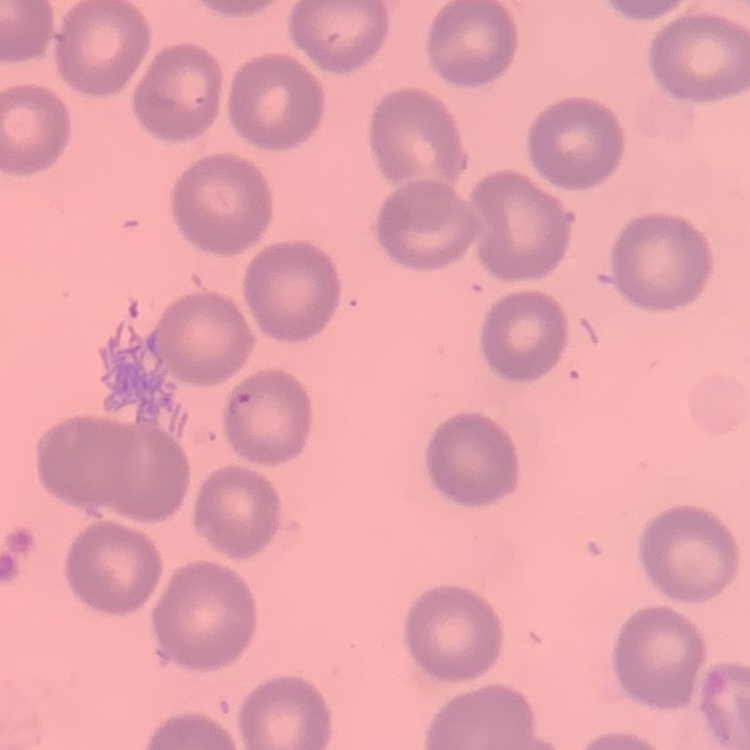

red_blood_cell_morphology: no rouleaux formation
image_type: one tile cut from a larger photomicrograph
stain: Field's or Giemsa
preparation: thin blood film